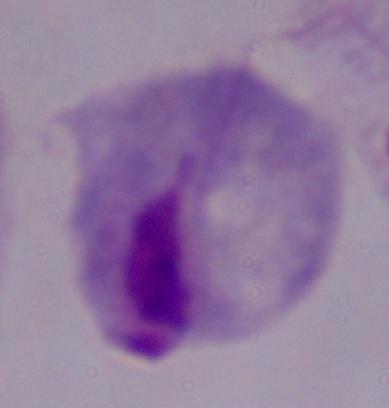

magnification = 1000x
modality = photomicrograph
identification = trichomonad